Assess the morphology of the red blood cells.
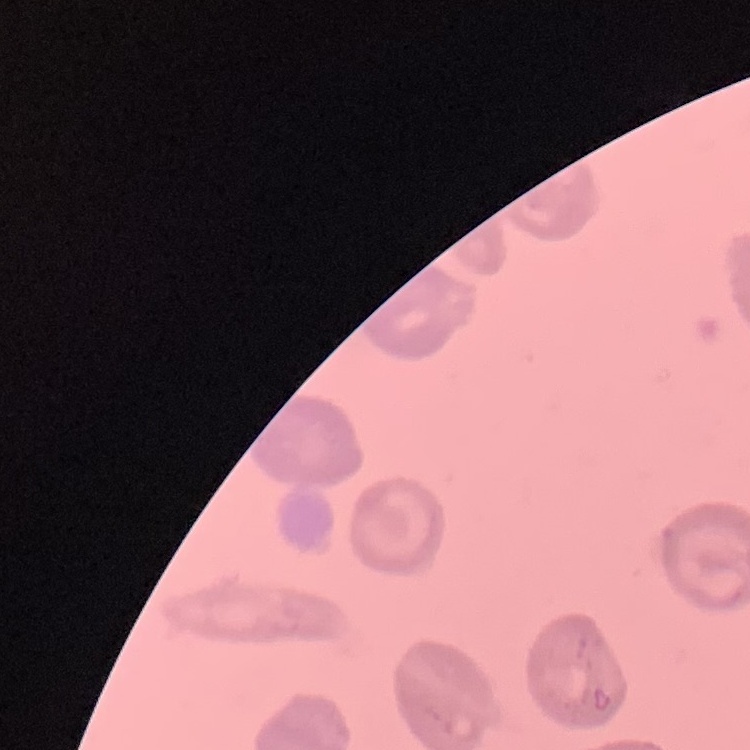

No rouleaux formation.

Summary:
  - Image type: square crop of a larger photomicrograph
  - Preparation: thin blood film
  - Stain: Field's or Giemsa